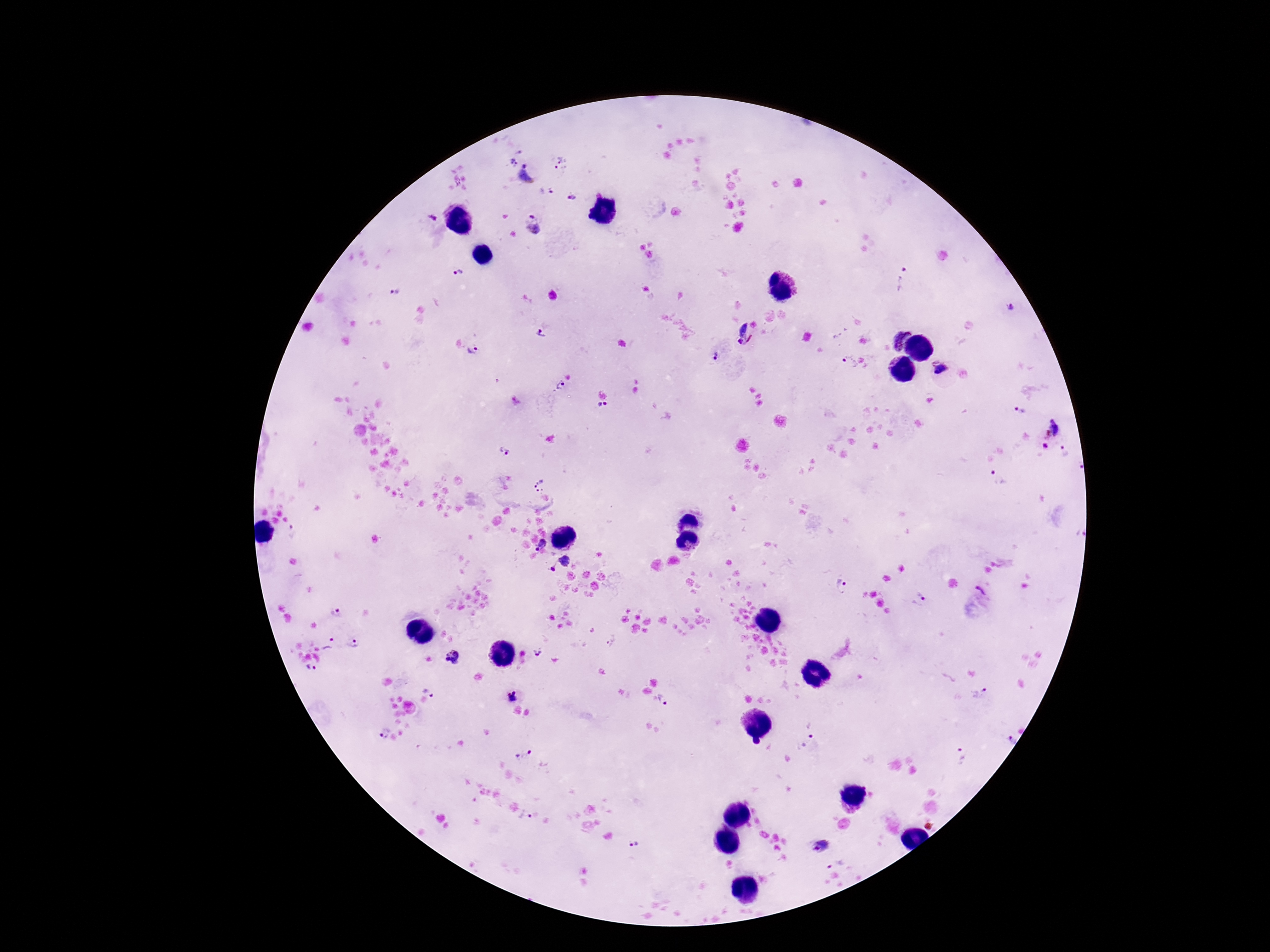

Approximate centers as [x, y] in pixels.
Summary:
  - Plasmodium parasite locations: [520, 152], [512, 162], [523, 164], [561, 165], [527, 177], [551, 191], [571, 198], [532, 216], [533, 230], [459, 273], [903, 281], [396, 295], [1010, 307], [743, 328], [541, 335], [750, 340], [903, 342], [741, 343], [473, 351], [715, 355], [850, 362], [939, 368], [560, 387], [602, 407], [1020, 410], [1057, 426], [1046, 447], [505, 451], [1064, 451], [998, 479], [541, 486], [541, 544], [568, 561], [552, 570], [842, 586], [981, 591], [919, 597], [336, 612], [612, 642], [330, 643], [353, 643], [540, 652], [454, 657], [311, 669], [431, 689], [510, 693], [980, 693], [659, 700], [382, 734], [1010, 740], [811, 742], [523, 753], [963, 756], [524, 815], [635, 843], [821, 846], [838, 862]
  - Image size: 1270×952 pixels
  - Preparation: thick blood smear
  - Magnification: 100x
  - Field of view: single
  - Patient malaria status: infected
  - Capture: smartphone camera through the microscope eyepiece
  - Stain: Giemsa